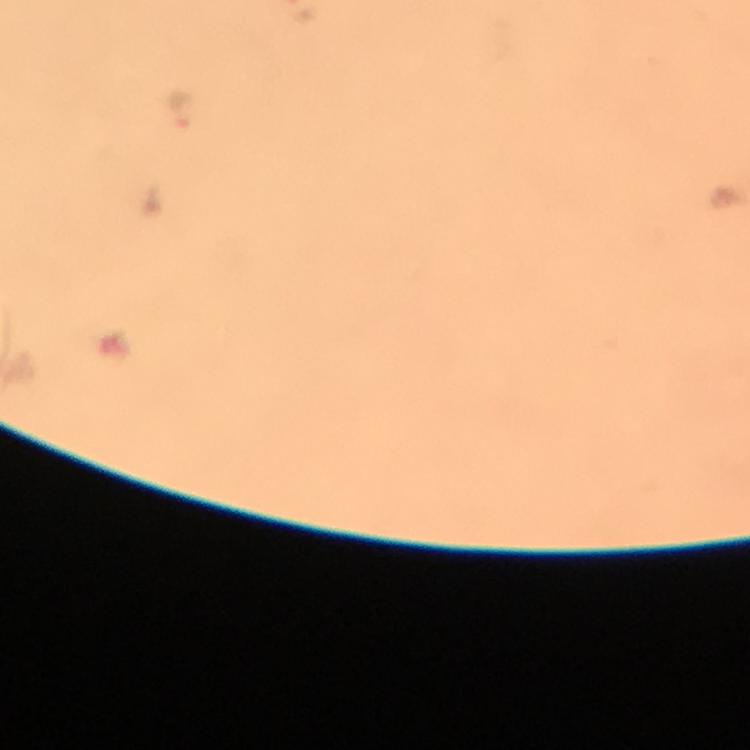
Approximate centers as (x, y) in pixels. Plasmodium parasite locations: (177, 110). 100x magnification. Immersion oil applied. Cropped region of a single field of view. Photographed through the microscope with a smartphone camera. From a malaria diagnostic workup. Giemsa-stained preparation. Thick blood smear. Image is 750×750 pixels.